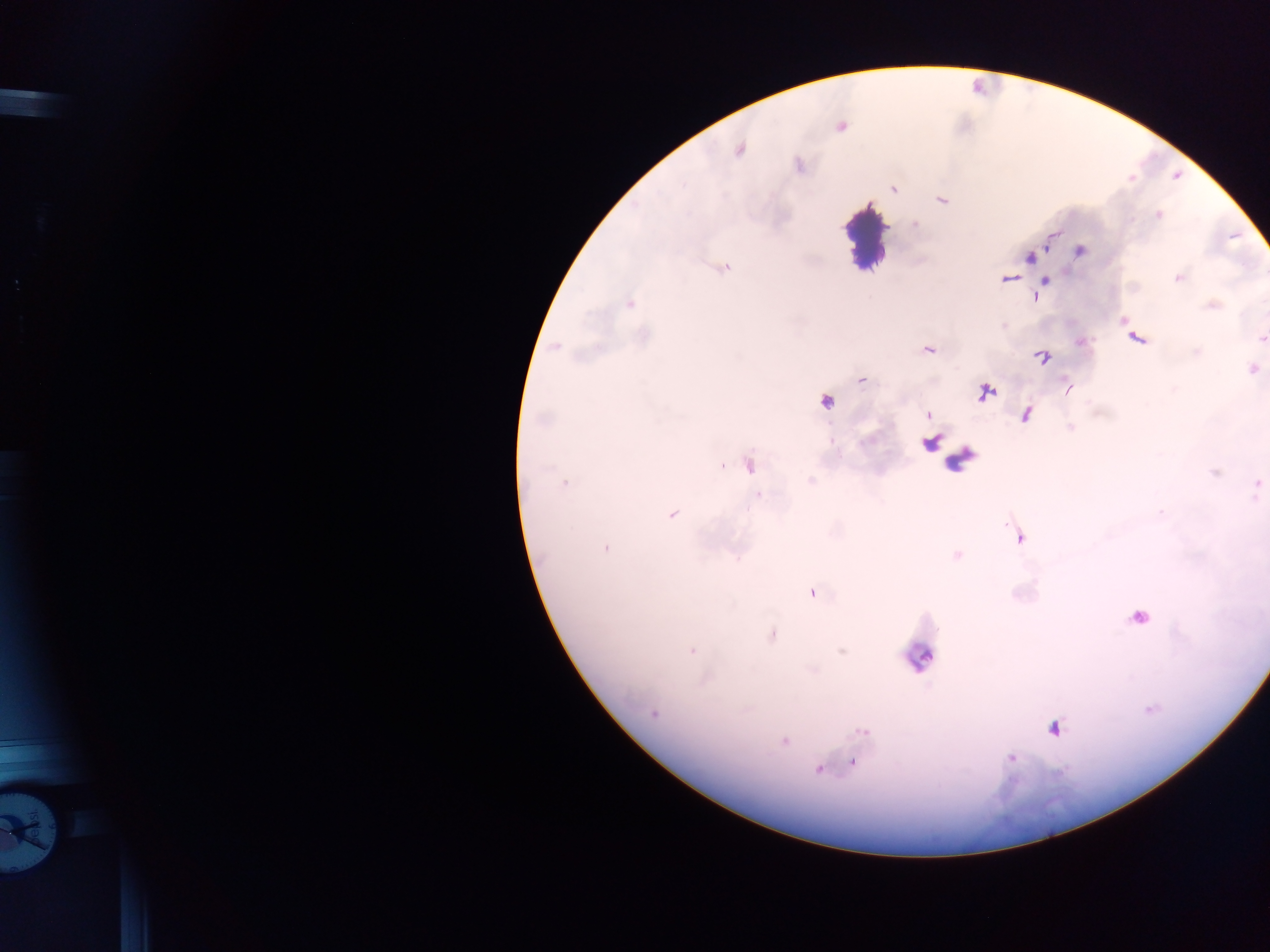

Approximate centers as {x, y} in pixels.
Summary:
  - Plasmodium parasite locations: {739, 150}, {894, 189}, {942, 199}, {1158, 214}, {1080, 251}, {1029, 257}, {726, 268}, {1178, 278}, {1008, 279}, {1045, 283}, {629, 304}, {1136, 338}, {1262, 339}, {555, 347}, {1042, 358}, {1253, 370}, {861, 380}, {1068, 390}, {987, 392}, {825, 402}, {927, 415}, {1027, 415}, {543, 420}, {930, 444}, {749, 465}, {721, 466}, {565, 483}, {1257, 484}, {759, 495}, {671, 515}, {1018, 536}, {605, 548}, {956, 555}, {812, 593}, {1139, 617}, {771, 635}, {692, 650}, {841, 651}, {1150, 709}, {653, 714}, {1054, 729}, {863, 731}, {784, 741}, {1011, 757}, {854, 764}, {818, 769}
  - Leukocyte locations: {864, 238}, {920, 656}, {35, 826}
  - Image size: 1270×952 pixels
  - Country: Ghana
  - Field of view: single
  - Preparation: thick blood smear
  - Capture: mobile-phone photograph through a microscope